Locate every blood parasite and identify its species.
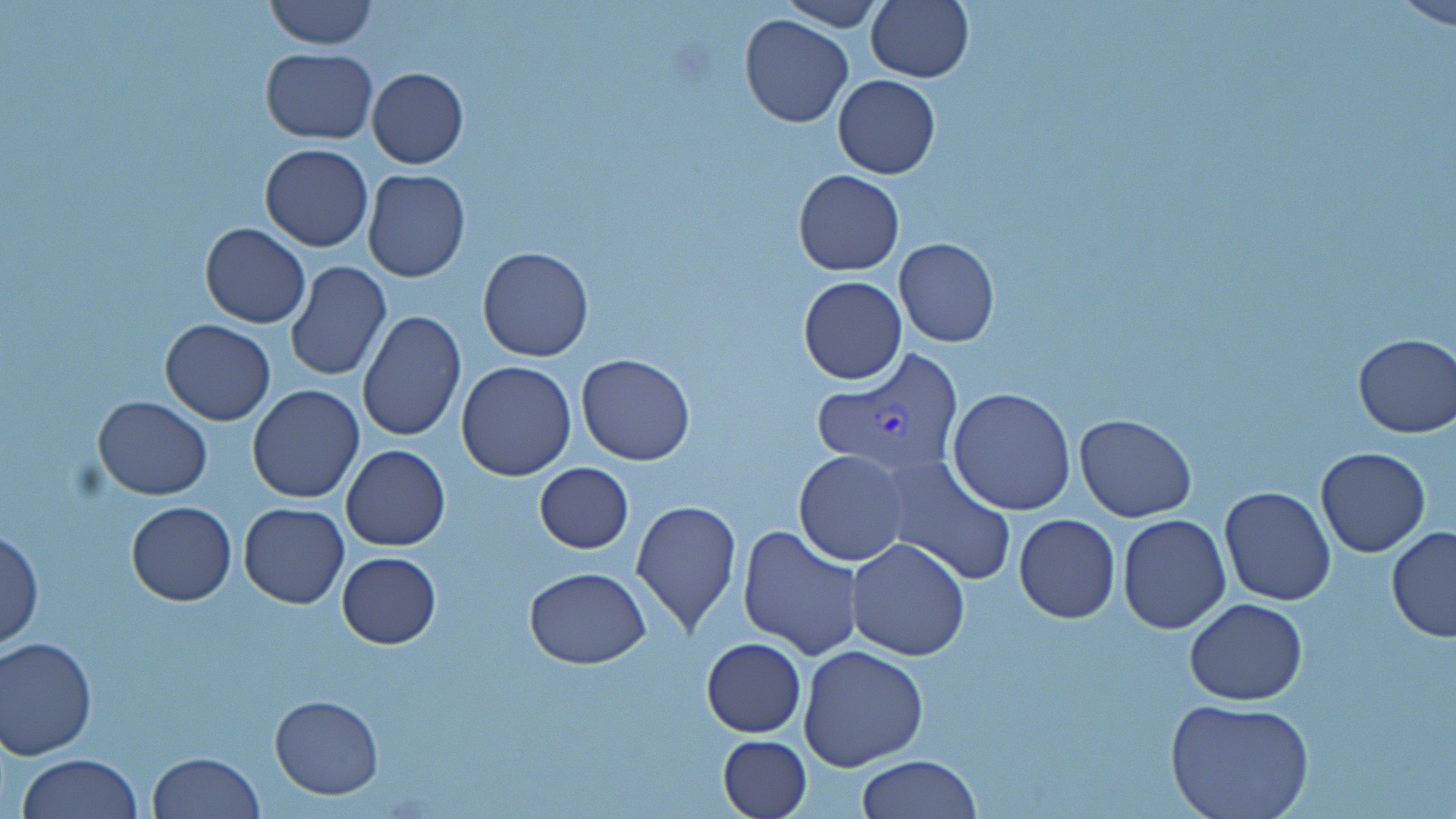

Approximate bounding boxes as named x1/y1/x2/y2 corners in pixels.
Plasmodium vivax-infected red blood cells: (x1=813, y1=349, x2=964, y2=483).
No Plasmodium falciparum, Plasmodium ovale, Plasmodium malariae, Babesia divergens, or Trypanosoma brucei observed.

slide-level diagnosis = Plasmodium vivax
image size = 1456×819 pixels
stain = May-Grünwald-Giemsa
magnification = 1000x
preparation = thin blood film
uninfected red blood cell locations = approximate bounding boxes as named x1/y1/x2/y2 corners in pixels: (x1=263, y1=0, x2=378, y2=50), (x1=774, y1=0, x2=885, y2=31), (x1=865, y1=0, x2=973, y2=82), (x1=1385, y1=0, x2=1456, y2=28), (x1=739, y1=14, x2=853, y2=128), (x1=261, y1=47, x2=378, y2=143), (x1=367, y1=67, x2=470, y2=168), (x1=833, y1=74, x2=941, y2=179), (x1=260, y1=142, x2=373, y2=251), (x1=361, y1=169, x2=471, y2=282), (x1=793, y1=169, x2=905, y2=276), (x1=201, y1=223, x2=310, y2=328), (x1=895, y1=239, x2=1000, y2=348), (x1=478, y1=247, x2=594, y2=362), (x1=284, y1=261, x2=391, y2=383), (x1=799, y1=276, x2=907, y2=384), (x1=356, y1=311, x2=466, y2=443), (x1=160, y1=318, x2=277, y2=425), (x1=1351, y1=333, x2=1455, y2=439), (x1=576, y1=353, x2=694, y2=465), (x1=455, y1=360, x2=577, y2=481), (x1=247, y1=385, x2=363, y2=502), (x1=949, y1=388, x2=1077, y2=515), (x1=93, y1=394, x2=212, y2=501), (x1=1075, y1=413, x2=1197, y2=522), (x1=342, y1=445, x2=451, y2=550), (x1=1316, y1=447, x2=1431, y2=558), (x1=795, y1=450, x2=908, y2=566), (x1=879, y1=457, x2=1018, y2=587), (x1=535, y1=463, x2=633, y2=553), (x1=1219, y1=485, x2=1336, y2=605), (x1=630, y1=499, x2=742, y2=635), (x1=126, y1=501, x2=236, y2=604), (x1=238, y1=501, x2=348, y2=608), (x1=1014, y1=514, x2=1121, y2=623), (x1=1117, y1=514, x2=1231, y2=634), (x1=737, y1=525, x2=863, y2=658), (x1=1386, y1=527, x2=1456, y2=641), (x1=1, y1=528, x2=43, y2=651), (x1=845, y1=537, x2=971, y2=661), (x1=336, y1=551, x2=441, y2=648), (x1=524, y1=568, x2=651, y2=669), (x1=1186, y1=599, x2=1309, y2=705), (x1=1, y1=636, x2=98, y2=758), (x1=701, y1=637, x2=806, y2=737), (x1=798, y1=643, x2=927, y2=772), (x1=269, y1=694, x2=383, y2=799), (x1=1165, y1=699, x2=1314, y2=819), (x1=718, y1=734, x2=812, y2=819), (x1=148, y1=750, x2=264, y2=819), (x1=17, y1=753, x2=144, y2=818), (x1=857, y1=754, x2=982, y2=818)
modality = optical microscopy
field of view = one of a larger specimen